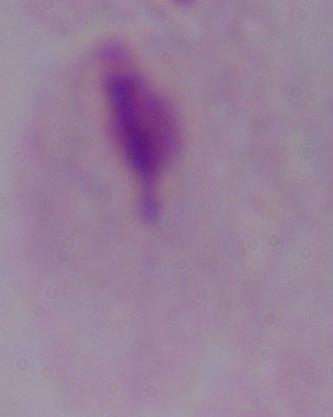
{
  "modality": "micrograph",
  "magnification": "1000x",
  "identification": "trichomonad"
}